Classify this cell by malaria status.
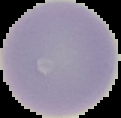

Uninfected.

preparation = thin blood smear
image type = cell region segmented out of the field of view; surrounding area masked to black
image size = 121×118 pixels